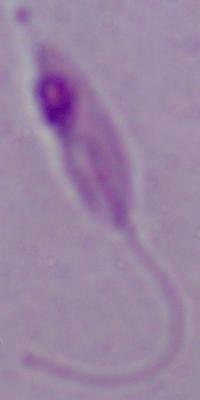

A Leishmania parasite is shown. 1000x magnification. Photomicrograph.